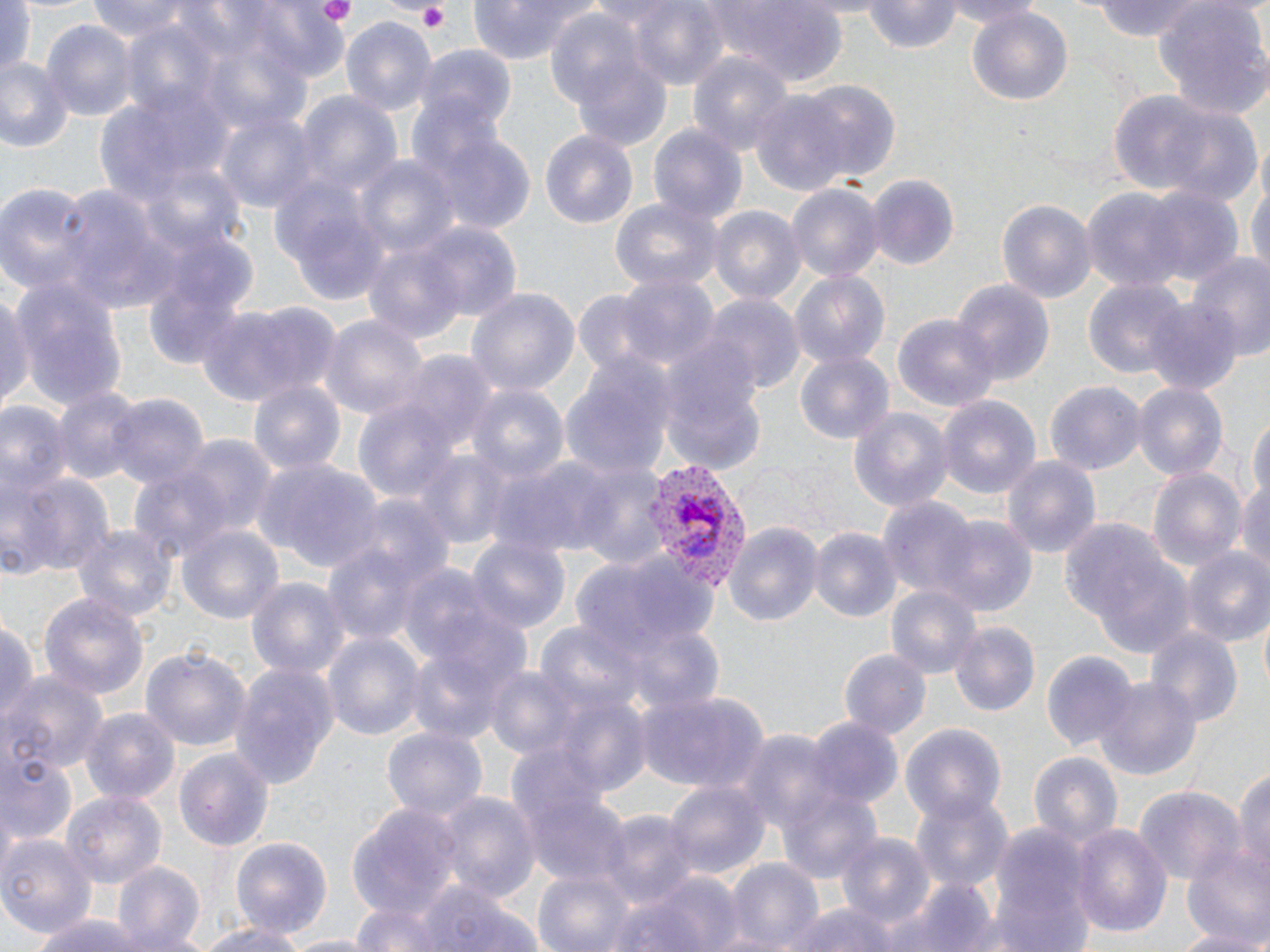

Summary:
  - Coordinate format: approximate bounding boxes as (x1, y1, x2, y2) in pixels
  - Platelet locations: (314, 0, 356, 26), (414, 3, 454, 33)
  - Uninfected red blood cell locations: (86, 0, 207, 42), (240, 0, 352, 85), (467, 0, 597, 63), (624, 0, 729, 92), (703, 0, 850, 81), (862, 0, 963, 51), (936, 0, 1044, 26), (1084, 1, 1218, 41), (1156, 1, 1270, 117), (0, 5, 50, 81), (966, 6, 1073, 110), (544, 10, 649, 114), (340, 16, 435, 114), (41, 20, 135, 122), (417, 47, 517, 134), (688, 51, 793, 160), (573, 54, 673, 151), (0, 58, 75, 153), (795, 80, 900, 182), (100, 87, 233, 202), (294, 89, 401, 203), (1101, 91, 1228, 204), (751, 93, 848, 195), (1155, 98, 1262, 209), (217, 111, 318, 213), (410, 116, 535, 237), (648, 124, 746, 225), (541, 130, 637, 231), (354, 154, 461, 263), (1246, 169, 1270, 292), (867, 173, 960, 270), (0, 180, 91, 298), (56, 181, 177, 314), (270, 182, 387, 302), (786, 183, 884, 287), (1140, 188, 1244, 286), (1081, 189, 1190, 295), (608, 195, 725, 296), (995, 197, 1096, 306), (707, 203, 805, 305), (415, 223, 522, 325), (359, 237, 476, 347), (1187, 249, 1270, 363), (788, 270, 890, 372), (146, 271, 252, 370), (614, 273, 717, 372), (10, 276, 129, 416), (953, 277, 1056, 384), (1083, 279, 1187, 380), (1, 286, 34, 408), (467, 289, 580, 400), (703, 296, 803, 398), (1143, 299, 1242, 393), (197, 300, 335, 406), (892, 314, 998, 414), (320, 315, 427, 420), (657, 346, 766, 474), (388, 351, 495, 453), (795, 352, 892, 445), (559, 359, 675, 476), (246, 375, 346, 479), (1132, 381, 1229, 483), (1045, 383, 1144, 474), (465, 385, 569, 487), (51, 386, 145, 488), (103, 393, 209, 494), (935, 394, 1041, 499), (0, 399, 71, 503), (354, 401, 460, 507), (847, 408, 952, 512), (1246, 414, 1270, 518), (180, 436, 277, 539), (412, 447, 513, 547), (490, 454, 614, 557), (1002, 455, 1101, 561), (250, 456, 383, 574), (1235, 459, 1270, 584), (569, 460, 667, 570), (128, 466, 236, 568), (1148, 467, 1246, 578), (4, 469, 116, 578), (881, 497, 981, 605), (939, 515, 1036, 617), (1059, 517, 1194, 653), (73, 522, 178, 626), (723, 522, 822, 627), (178, 524, 285, 626), (807, 527, 899, 622), (466, 536, 569, 638), (321, 539, 427, 650), (1182, 547, 1270, 649), (579, 550, 720, 657), (398, 564, 501, 667), (246, 575, 348, 684), (887, 584, 981, 680), (39, 592, 150, 705), (0, 614, 38, 730), (534, 622, 649, 725), (950, 622, 1039, 716), (1145, 627, 1241, 732), (404, 632, 522, 748), (324, 633, 422, 740), (140, 644, 252, 750), (839, 648, 931, 739), (1040, 649, 1138, 753), (225, 662, 339, 793), (483, 664, 588, 757), (3, 670, 109, 776), (1095, 675, 1201, 783), (637, 691, 768, 793), (81, 708, 179, 805), (804, 717, 902, 812), (899, 721, 1007, 823), (383, 727, 487, 827), (737, 730, 840, 843), (175, 744, 275, 852), (1028, 751, 1124, 855), (0, 752, 75, 852), (1233, 759, 1269, 888), (516, 778, 629, 891), (663, 780, 771, 883), (778, 785, 883, 887), (1133, 785, 1242, 890), (435, 790, 539, 904), (908, 790, 1012, 892), (62, 793, 165, 888), (347, 803, 465, 921), (597, 810, 696, 909), (1071, 821, 1172, 940), (989, 824, 1092, 948), (0, 830, 98, 939), (835, 831, 937, 932), (230, 836, 332, 941), (1183, 846, 1270, 951), (720, 858, 823, 948), (108, 859, 207, 950), (531, 869, 635, 950), (612, 869, 746, 952), (898, 877, 996, 952), (388, 880, 544, 952), (348, 900, 461, 951), (784, 900, 900, 952), (30, 911, 148, 952), (189, 919, 316, 952), (1164, 926, 1269, 951), (276, 934, 378, 952)
  - Plasmodium vivax-infected red blood cell locations: (640, 459, 744, 592)
  - Slide-level diagnosis: Plasmodium vivax
  - Modality: light microscopy
  - Image size: 1270×952 pixels
  - Preparation: thin blood smear
  - Field of view: single
  - Stain: May-Grünwald-Giemsa
  - Magnification: 1000x